Assess this cell for malaria.
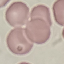
Uninfected.

image_type: automatically extracted cell patch, resized to 64 × 64 pixels
preparation: thin blood film
stain: Giemsa
capture: smartphone camera at the microscope eyepiece